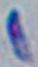 Toxoplasma gondii is shown. Photomicrograph. Captured at 1000x magnification.